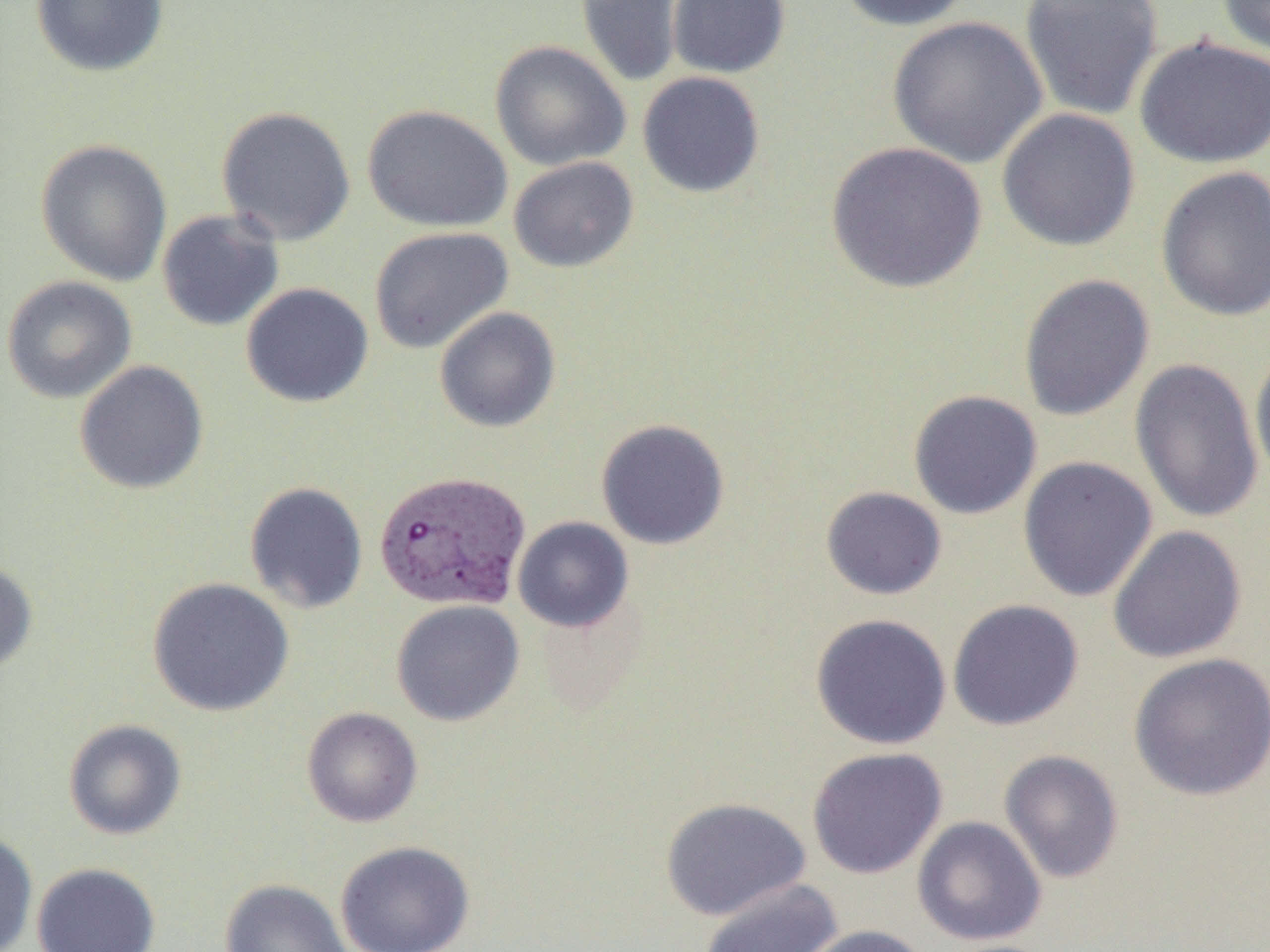

slide_level_diagnosis: Plasmodium vivax
magnification: 1000x
uninfected_red_blood_cell_locations: 'approximate bounding boxes as (x1,y1)-(x2,y2) corner pairs in pixels: (31,0)-(169,77), (667,0)-(790,78), (835,0)-(976,32), (1019,0)-(1164,121), (1216,0)-(1270,59), (575,1)-(684,88), (887,16)-(1048,168), (1134,35)-(1270,168), (489,40)-(631,172), (637,71)-(765,198), (361,104)-(513,233), (216,106)-(356,246), (996,108)-(1141,251), (35,139)-(172,287), (825,141)-(987,293), (508,156)-(639,273), (1155,165)-(1270,322), (156,209)-(285,332), (369,226)-(513,353), (1018,273)-(1155,422), (1,275)-(137,404), (240,282)-(374,408), (434,306)-(561,432), (1249,340)-(1270,487), (1129,357)-(1264,525), (74,360)-(209,495), (908,390)-(1042,520), (596,418)-(730,549), (1017,455)-(1158,602), (244,481)-(368,614), (820,486)-(947,600), (512,516)-(634,633), (1107,525)-(1247,664), (0,558)-(38,675), (146,577)-(295,716), (391,599)-(525,726), (947,599)-(1084,731), (810,613)-(952,750), (1127,651)-(1270,802), (302,706)-(423,827), (63,719)-(187,840), (807,747)-(947,879), (999,749)-(1125,884), (659,796)-(811,921), (912,816)-(1047,946), (0,830)-(38,952), (334,840)-(475,952), (32,862)-(161,952), (699,878)-(843,952), (220,879)-(352,952), (797,924)-(932,952)'
plasmodium_vivax_infected_red_blood_cell_locations: 'approximate bounding boxes as (x1,y1)-(x2,y2) corner pairs in pixels: (374,469)-(531,612)'
image_size: 1270×952 pixels
modality: optical microscopy
preparation: thin blood film
field_of_view: single